Comment on the morphology of the erythrocytes.
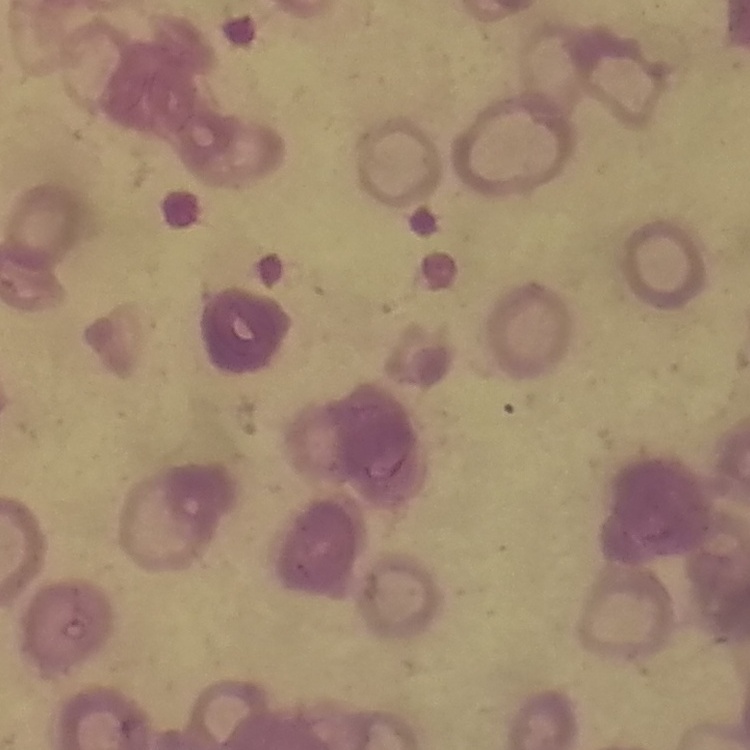
They show rouleaux formation.

One tile cut from a larger photomicrograph. Stained with either Field's or Giemsa. Thin blood film.